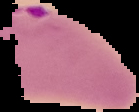

{
  "image_type": "segmented cell region on a black background",
  "malaria_status": "parasitized",
  "preparation": "thin blood smear",
  "image_size": "139×112 pixels"
}